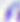

magnification = 400x
modality = photomicrograph
identification = Toxoplasma gondii